Report the malaria status of this cell.
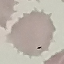
Uninfected.

capture = smartphone through the microscope eyepiece
preparation = thin blood film
stain = Giemsa
image type = cell patch, automatically extracted from a larger field of view and resized to 64 × 64 pixels